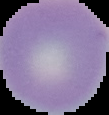

Segmented cell region on a black background. Image is 109×115 pixels. From a thin blood smear. Result: negative for Plasmodium parasites.